Locate every Plasmodium malariae-infected red blood cell.
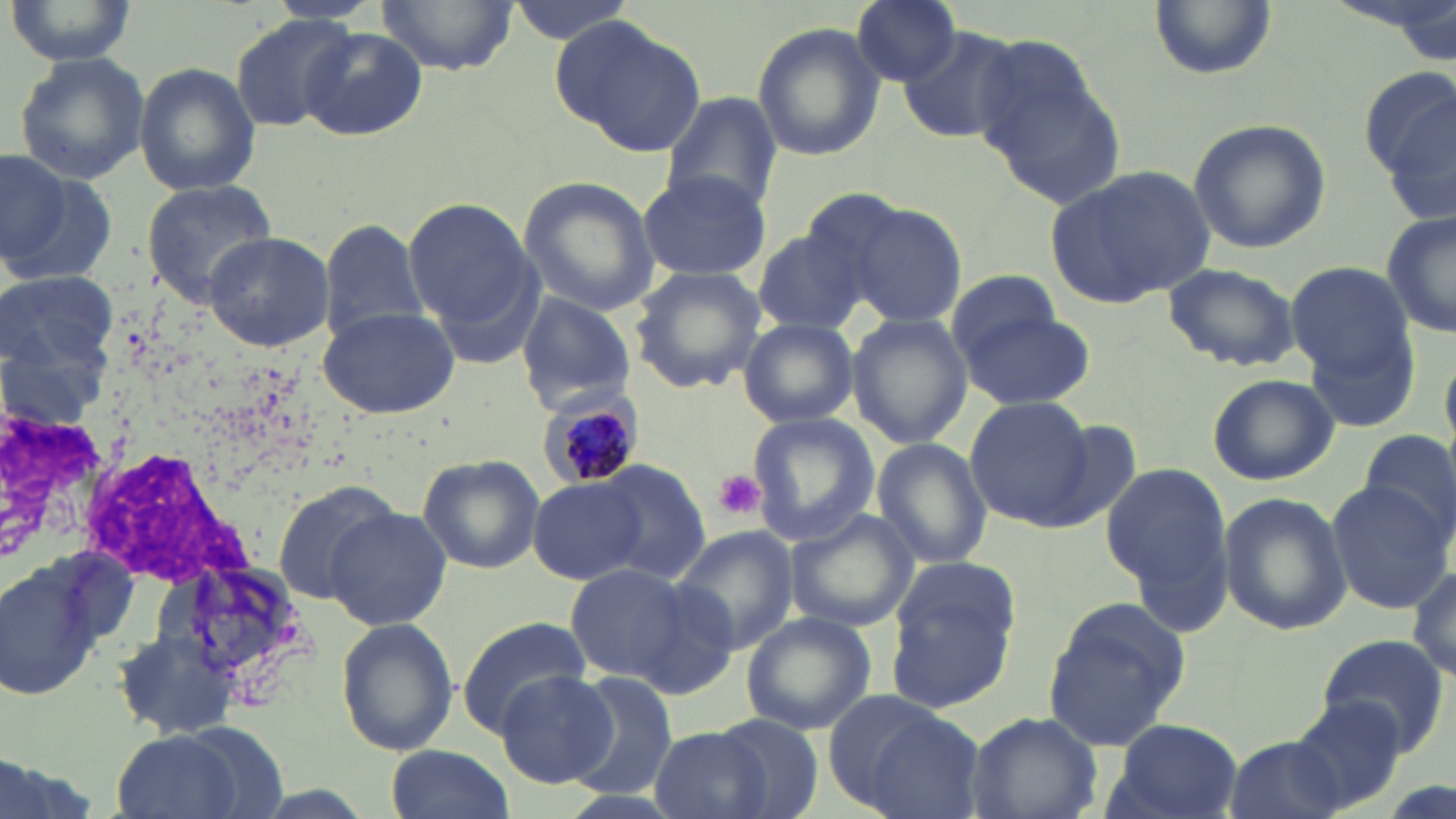

Approximate bounding boxes as (x1,y1)-(x2,y2) corner pairs in pixels.
Plasmodium malariae-infected red blood cells: (542,400)-(642,490).

Summary:
  - Uninfected red blood cell locations: (375,0)-(522,74), (500,0)-(639,44), (851,0)-(963,86), (1147,0)-(1278,78), (6,2)-(139,66), (228,13)-(362,133), (557,15)-(707,157), (752,21)-(885,163), (896,26)-(1024,145), (296,28)-(430,141), (980,51)-(1127,209), (14,52)-(151,184), (134,61)-(260,197), (1360,65)-(1456,226), (664,94)-(780,212), (1189,118)-(1330,254), (1,147)-(68,267), (1048,164)-(1213,308), (5,166)-(114,288), (638,171)-(769,282), (518,177)-(663,317), (141,180)-(275,301), (404,199)-(537,331), (844,201)-(967,328), (1380,209)-(1455,341), (320,219)-(431,348), (751,226)-(873,338), (202,231)-(334,352), (1286,259)-(1415,379), (1162,262)-(1299,371), (626,266)-(768,395), (946,270)-(1067,362), (1,272)-(116,394), (514,292)-(634,412), (315,304)-(462,419), (957,305)-(1095,410), (847,313)-(970,449), (1302,315)-(1423,431), (734,319)-(860,427), (1207,372)-(1339,486), (964,395)-(1097,529), (0,407)-(114,564), (746,412)-(880,546), (1360,428)-(1454,539), (871,436)-(992,571), (416,455)-(545,575), (1100,459)-(1236,612), (594,462)-(712,582), (529,476)-(646,583), (272,480)-(398,604), (1327,481)-(1451,613), (1218,492)-(1351,635), (323,506)-(454,630), (783,508)-(919,634), (672,525)-(800,653), (161,547)-(314,696), (1,555)-(106,704), (883,557)-(1025,711), (1408,561)-(1456,681), (564,564)-(694,683), (621,575)-(744,699), (1041,596)-(1193,754), (741,612)-(877,734), (334,615)-(459,758), (455,618)-(593,735), (113,629)-(236,741), (1317,631)-(1451,757), (493,669)-(617,789), (569,673)-(680,801), (825,694)-(983,816), (1287,701)-(1410,812), (968,711)-(1102,819), (711,712)-(824,819), (1105,717)-(1242,819), (648,725)-(772,819), (110,730)-(244,819), (1222,734)-(1348,819), (385,743)-(514,818), (0,749)-(100,819)
  - Platelet locations: (712,469)-(766,520)
  - Slide-level diagnosis: Plasmodium malariae
  - Stain: May-Grünwald-Giemsa
  - Modality: optical microscopy
  - Image size: 1456×819 pixels
  - Magnification: 1000x
  - Field of view: single
  - Preparation: thin blood film